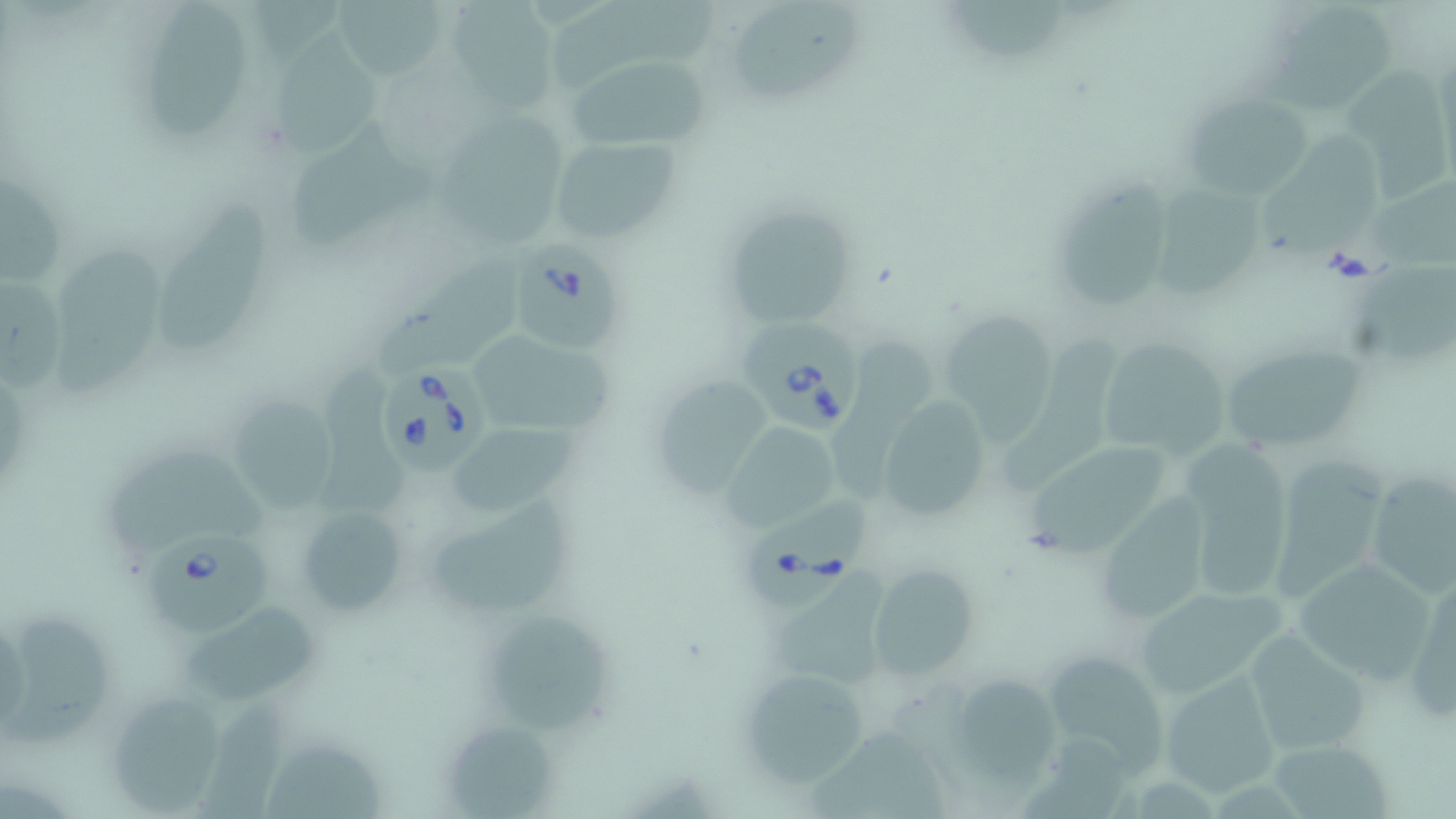
Summary:
  - Coordinate format: approximate bounding boxes as (x1,y1)-(x2,y2) corner pairs in pixels
  - Uninfected red blood cell locations: (442,0)-(562,112), (551,0)-(731,88), (726,0)-(864,106), (151,1)-(253,145), (328,1)-(450,79), (950,3)-(1077,71), (1270,5)-(1397,114), (276,23)-(384,158), (562,54)-(711,151), (1343,59)-(1448,207), (1181,92)-(1318,201), (433,109)-(572,252), (289,116)-(436,250), (1273,132)-(1382,264), (548,136)-(680,246), (1058,174)-(1172,312), (1367,175)-(1449,276), (1158,176)-(1262,301), (1,179)-(69,291), (162,194)-(278,355), (722,204)-(859,334), (56,241)-(171,400), (379,245)-(525,373), (1356,261)-(1450,366), (1,279)-(65,393), (949,312)-(1057,442), (1004,324)-(1121,491), (462,326)-(614,439), (842,334)-(938,498), (1095,338)-(1233,463), (1219,344)-(1371,455), (321,363)-(417,521), (653,377)-(775,499), (877,395)-(990,522), (225,396)-(338,512), (443,418)-(577,522), (719,420)-(845,529), (108,433)-(271,562), (1166,440)-(1295,608), (1035,442)-(1169,558), (1271,451)-(1382,608), (1363,470)-(1455,599), (1107,486)-(1214,623), (428,500)-(590,612), (295,504)-(409,618), (1288,556)-(1443,683), (864,565)-(981,681), (1408,570)-(1456,727), (1132,584)-(1288,700), (7,613)-(113,752), (184,613)-(326,704), (485,614)-(620,735), (1242,629)-(1372,757), (1050,652)-(1165,782), (735,667)-(874,788), (1158,670)-(1286,800), (965,671)-(1069,793), (102,688)-(233,815), (203,700)-(281,819), (443,719)-(555,815), (810,721)-(954,819), (1265,737)-(1397,819), (262,743)-(390,819)
  - Babesia divergens-infected red blood cell locations: (517,240)-(626,354), (735,319)-(863,433), (381,358)-(490,474), (743,496)-(869,614), (143,530)-(271,636)
  - Slide-level diagnosis: Babesia divergens
  - Modality: light microscopy
  - Preparation: thin blood film
  - Magnification: 1000x
  - Field of view: single
  - Stain: May-Grünwald-Giemsa
  - Image size: 1456×819 pixels